Evaluate for Plasmodium parasites.
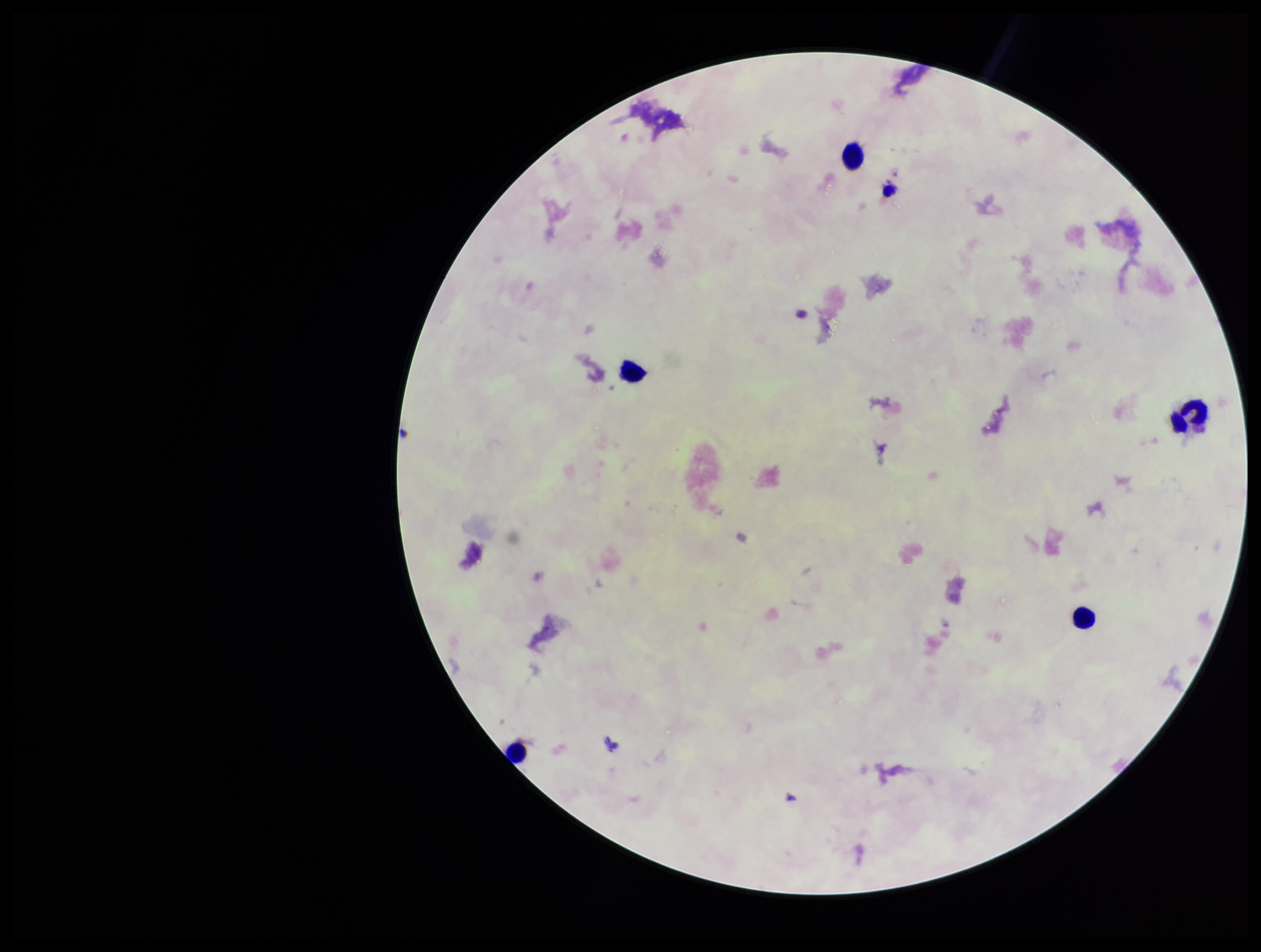
None identified.

leukocyte count = 5
capture = smartphone photograph through the microscope eyepiece
preparation = thick smear
stain = Giemsa
patient malaria status = negative
image size = 1261×952 pixels
field of view = single
parasite count = 0